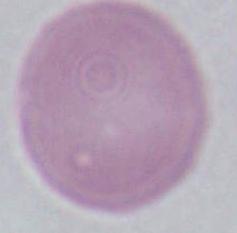 Captured at 1000x magnification. Micrograph. An erythrocyte is seen.